Give the preparation type.
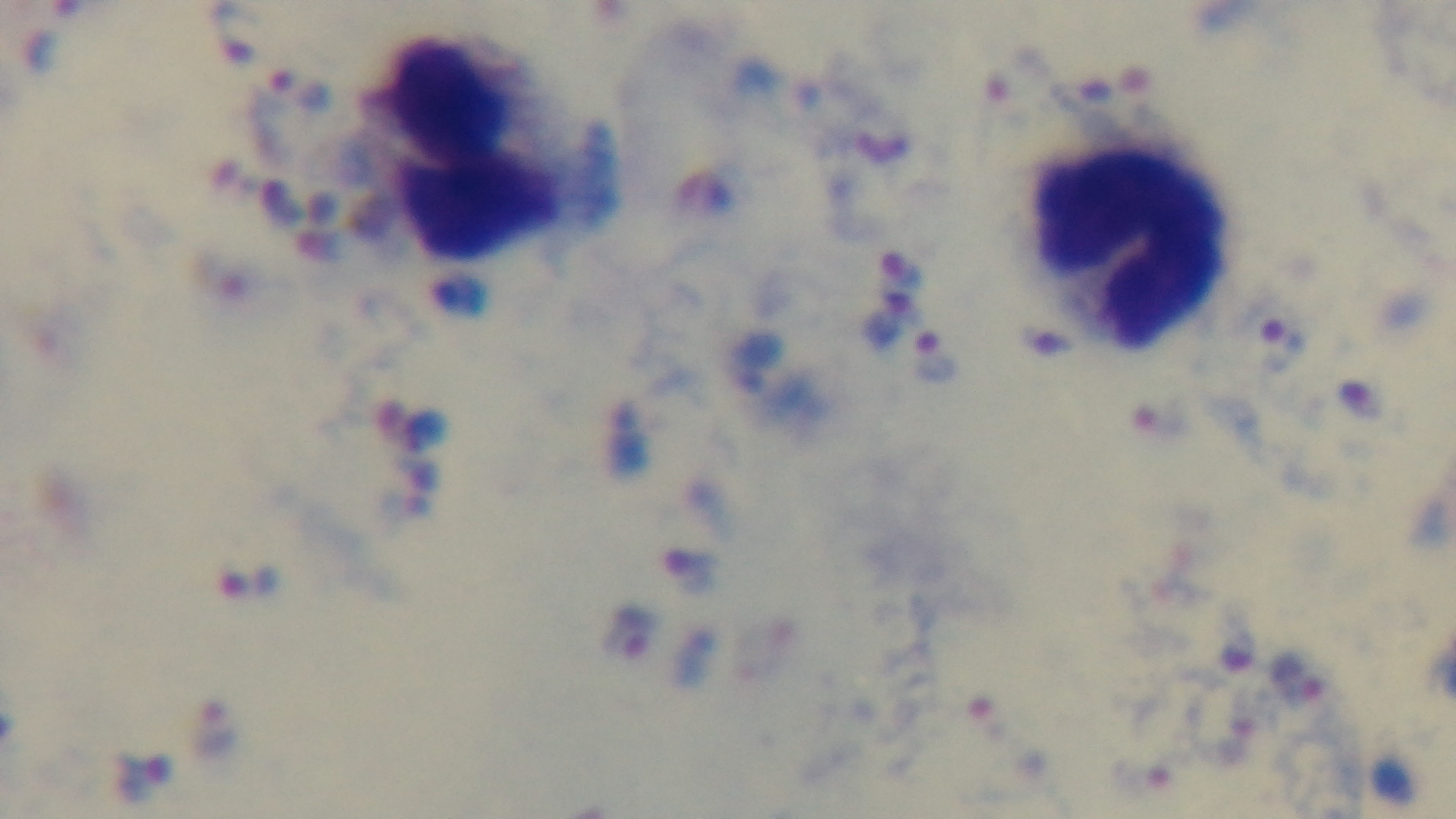
Thick.

objective = 100x oil immersion
field of view = single
modality = light microscopy
capture = mounted 4K digital camera
malaria status = positive
stain = Giemsa